Describe the morphology of the red blood cells.
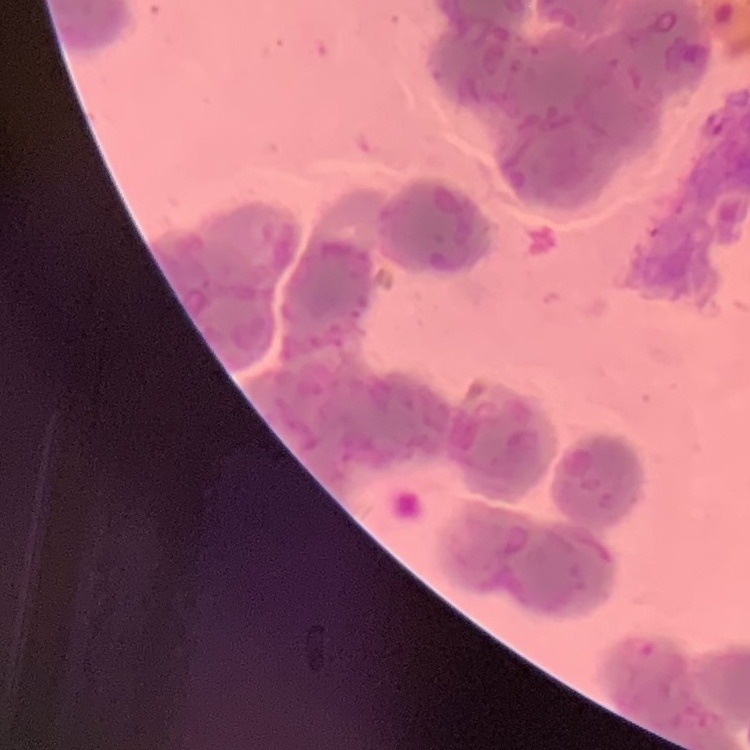
They show rouleaux formation.

{
  "preparation": "thin peripheral smear",
  "image_type": "one tile cut from a larger photomicrograph",
  "stain": "Field's or Giemsa"
}